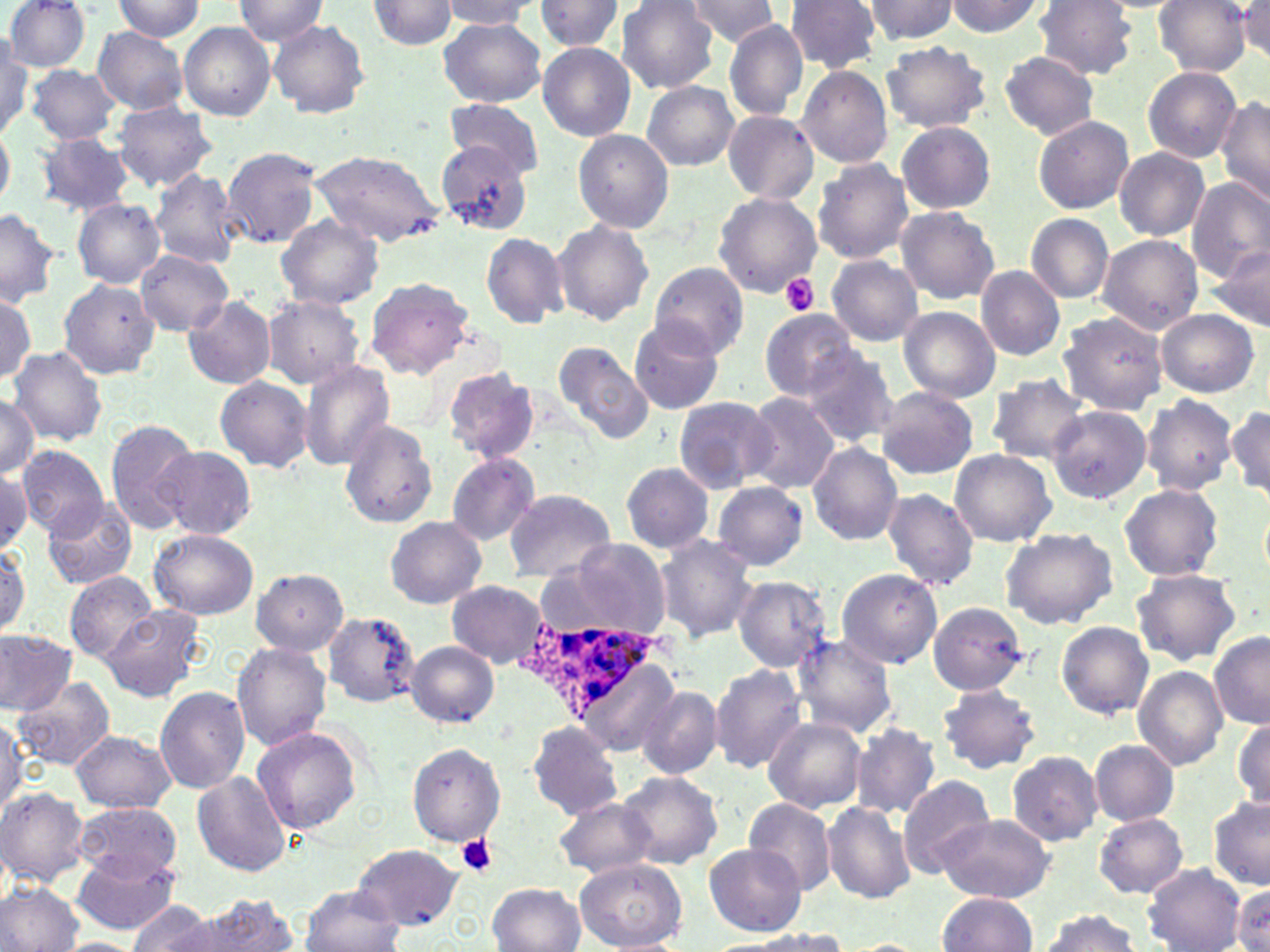

Summary:
  - Coordinate format: approximate bounding boxes as named x1/y1/x2/y2 corners in pixels
  - Plasmodium ovale-infected red blood cell locations: (x1=528, y1=618, x2=660, y2=727)
  - Uninfected red blood cell locations: (x1=2, y1=0, x2=90, y2=72), (x1=113, y1=0, x2=205, y2=41), (x1=233, y1=0, x2=329, y2=46), (x1=616, y1=0, x2=721, y2=92), (x1=685, y1=0, x2=779, y2=45), (x1=787, y1=0, x2=881, y2=74), (x1=860, y1=0, x2=962, y2=44), (x1=943, y1=0, x2=1046, y2=40), (x1=1034, y1=0, x2=1139, y2=79), (x1=1156, y1=0, x2=1252, y2=75), (x1=369, y1=1, x2=459, y2=48), (x1=438, y1=1, x2=541, y2=32), (x1=534, y1=1, x2=626, y2=53), (x1=1236, y1=3, x2=1270, y2=62), (x1=267, y1=19, x2=370, y2=119), (x1=439, y1=19, x2=546, y2=107), (x1=722, y1=19, x2=809, y2=121), (x1=179, y1=22, x2=276, y2=120), (x1=92, y1=27, x2=189, y2=115), (x1=1, y1=39, x2=33, y2=138), (x1=881, y1=41, x2=990, y2=134), (x1=538, y1=44, x2=636, y2=140), (x1=997, y1=50, x2=1100, y2=140), (x1=24, y1=64, x2=122, y2=143), (x1=796, y1=66, x2=893, y2=169), (x1=1143, y1=66, x2=1241, y2=162), (x1=642, y1=81, x2=739, y2=171), (x1=1216, y1=95, x2=1270, y2=207), (x1=113, y1=100, x2=216, y2=190), (x1=444, y1=101, x2=544, y2=176), (x1=722, y1=110, x2=818, y2=204), (x1=1032, y1=115, x2=1134, y2=214), (x1=897, y1=121, x2=995, y2=214), (x1=0, y1=127, x2=13, y2=208), (x1=573, y1=130, x2=672, y2=233), (x1=37, y1=132, x2=135, y2=215), (x1=436, y1=142, x2=535, y2=236), (x1=1115, y1=147, x2=1210, y2=240), (x1=221, y1=148, x2=322, y2=248), (x1=308, y1=148, x2=445, y2=249), (x1=811, y1=158, x2=914, y2=266), (x1=149, y1=168, x2=242, y2=268), (x1=1185, y1=178, x2=1270, y2=283), (x1=713, y1=192, x2=821, y2=298), (x1=71, y1=198, x2=165, y2=288), (x1=895, y1=206, x2=999, y2=304), (x1=0, y1=208, x2=62, y2=306), (x1=1025, y1=213, x2=1115, y2=303), (x1=275, y1=214, x2=383, y2=310), (x1=551, y1=218, x2=654, y2=326), (x1=481, y1=233, x2=568, y2=326), (x1=1097, y1=235, x2=1204, y2=334), (x1=1207, y1=247, x2=1270, y2=333), (x1=136, y1=250, x2=233, y2=334), (x1=826, y1=255, x2=924, y2=345), (x1=648, y1=261, x2=750, y2=360), (x1=975, y1=265, x2=1066, y2=360), (x1=363, y1=276, x2=476, y2=379), (x1=58, y1=277, x2=160, y2=377), (x1=0, y1=292, x2=36, y2=383), (x1=262, y1=294, x2=363, y2=389), (x1=182, y1=295, x2=276, y2=389), (x1=899, y1=307, x2=1000, y2=402), (x1=1155, y1=309, x2=1260, y2=398), (x1=759, y1=310, x2=861, y2=400), (x1=1057, y1=312, x2=1168, y2=415), (x1=629, y1=318, x2=727, y2=415), (x1=552, y1=340, x2=656, y2=447), (x1=800, y1=346, x2=898, y2=446), (x1=9, y1=347, x2=105, y2=444), (x1=296, y1=358, x2=397, y2=470), (x1=443, y1=366, x2=538, y2=463), (x1=214, y1=375, x2=313, y2=471), (x1=987, y1=375, x2=1088, y2=464), (x1=875, y1=386, x2=979, y2=480), (x1=0, y1=393, x2=40, y2=479), (x1=740, y1=393, x2=840, y2=494), (x1=673, y1=395, x2=776, y2=492), (x1=1141, y1=396, x2=1236, y2=495), (x1=1047, y1=405, x2=1152, y2=504), (x1=1228, y1=406, x2=1270, y2=500), (x1=105, y1=419, x2=198, y2=533), (x1=338, y1=420, x2=439, y2=528), (x1=807, y1=443, x2=903, y2=546), (x1=17, y1=446, x2=108, y2=538), (x1=156, y1=446, x2=257, y2=539), (x1=949, y1=449, x2=1057, y2=547), (x1=446, y1=454, x2=539, y2=546), (x1=620, y1=461, x2=714, y2=555), (x1=0, y1=467, x2=33, y2=554), (x1=713, y1=481, x2=807, y2=571), (x1=1119, y1=484, x2=1221, y2=581), (x1=881, y1=488, x2=978, y2=590), (x1=504, y1=489, x2=615, y2=582), (x1=44, y1=499, x2=138, y2=590), (x1=385, y1=515, x2=485, y2=609), (x1=148, y1=529, x2=258, y2=620), (x1=1001, y1=529, x2=1115, y2=629), (x1=653, y1=536, x2=758, y2=641), (x1=553, y1=538, x2=675, y2=640), (x1=0, y1=541, x2=29, y2=637), (x1=250, y1=568, x2=348, y2=655), (x1=836, y1=568, x2=943, y2=669), (x1=1129, y1=568, x2=1242, y2=667), (x1=64, y1=571, x2=159, y2=663), (x1=731, y1=575, x2=831, y2=673), (x1=447, y1=581, x2=548, y2=667), (x1=927, y1=601, x2=1031, y2=696), (x1=101, y1=605, x2=205, y2=703), (x1=324, y1=610, x2=423, y2=709), (x1=1056, y1=621, x2=1153, y2=719), (x1=0, y1=628, x2=77, y2=715), (x1=790, y1=631, x2=895, y2=739), (x1=1209, y1=632, x2=1270, y2=729), (x1=405, y1=641, x2=499, y2=727), (x1=231, y1=642, x2=330, y2=751), (x1=708, y1=666, x2=806, y2=772), (x1=1134, y1=666, x2=1227, y2=770), (x1=13, y1=675, x2=115, y2=769), (x1=937, y1=682, x2=1040, y2=773), (x1=638, y1=686, x2=722, y2=781), (x1=154, y1=687, x2=249, y2=792), (x1=0, y1=715, x2=29, y2=815), (x1=764, y1=717, x2=867, y2=813), (x1=1233, y1=719, x2=1269, y2=809), (x1=525, y1=721, x2=625, y2=820), (x1=850, y1=722, x2=942, y2=820), (x1=251, y1=726, x2=364, y2=836), (x1=70, y1=729, x2=177, y2=812), (x1=1089, y1=738, x2=1177, y2=827), (x1=406, y1=742, x2=506, y2=845), (x1=1007, y1=752, x2=1104, y2=845), (x1=192, y1=771, x2=293, y2=877), (x1=618, y1=771, x2=723, y2=869), (x1=896, y1=774, x2=997, y2=879), (x1=0, y1=787, x2=89, y2=887), (x1=553, y1=797, x2=658, y2=878), (x1=743, y1=797, x2=837, y2=896), (x1=1209, y1=798, x2=1270, y2=891), (x1=821, y1=801, x2=914, y2=903), (x1=74, y1=802, x2=184, y2=884), (x1=1094, y1=813, x2=1188, y2=897), (x1=934, y1=814, x2=1053, y2=903), (x1=353, y1=843, x2=463, y2=928), (x1=705, y1=845, x2=804, y2=934), (x1=70, y1=853, x2=179, y2=935), (x1=573, y1=858, x2=688, y2=951), (x1=1143, y1=864, x2=1246, y2=951), (x1=1, y1=882, x2=85, y2=952), (x1=488, y1=883, x2=584, y2=951), (x1=301, y1=885, x2=404, y2=952), (x1=1231, y1=887, x2=1270, y2=950), (x1=937, y1=893, x2=1037, y2=951), (x1=193, y1=894, x2=300, y2=950), (x1=128, y1=901, x2=221, y2=951), (x1=1036, y1=910, x2=1142, y2=951), (x1=732, y1=932, x2=850, y2=952), (x1=59, y1=937, x2=140, y2=951), (x1=839, y1=939, x2=931, y2=951)
  - Platelet locations: (x1=779, y1=275, x2=819, y2=316), (x1=456, y1=835, x2=499, y2=876)
  - Slide-level diagnosis: Plasmodium ovale
  - Modality: optical microscopy
  - Field of view: single
  - Magnification: 1000x
  - Image size: 1270×952 pixels
  - Preparation: thin blood smear
  - Stain: May-Grünwald-Giemsa